Name the parasite shown.
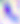
Toxoplasma gondii.

modality = micrograph
magnification = 400x